Locate every Trypanosoma brucei.
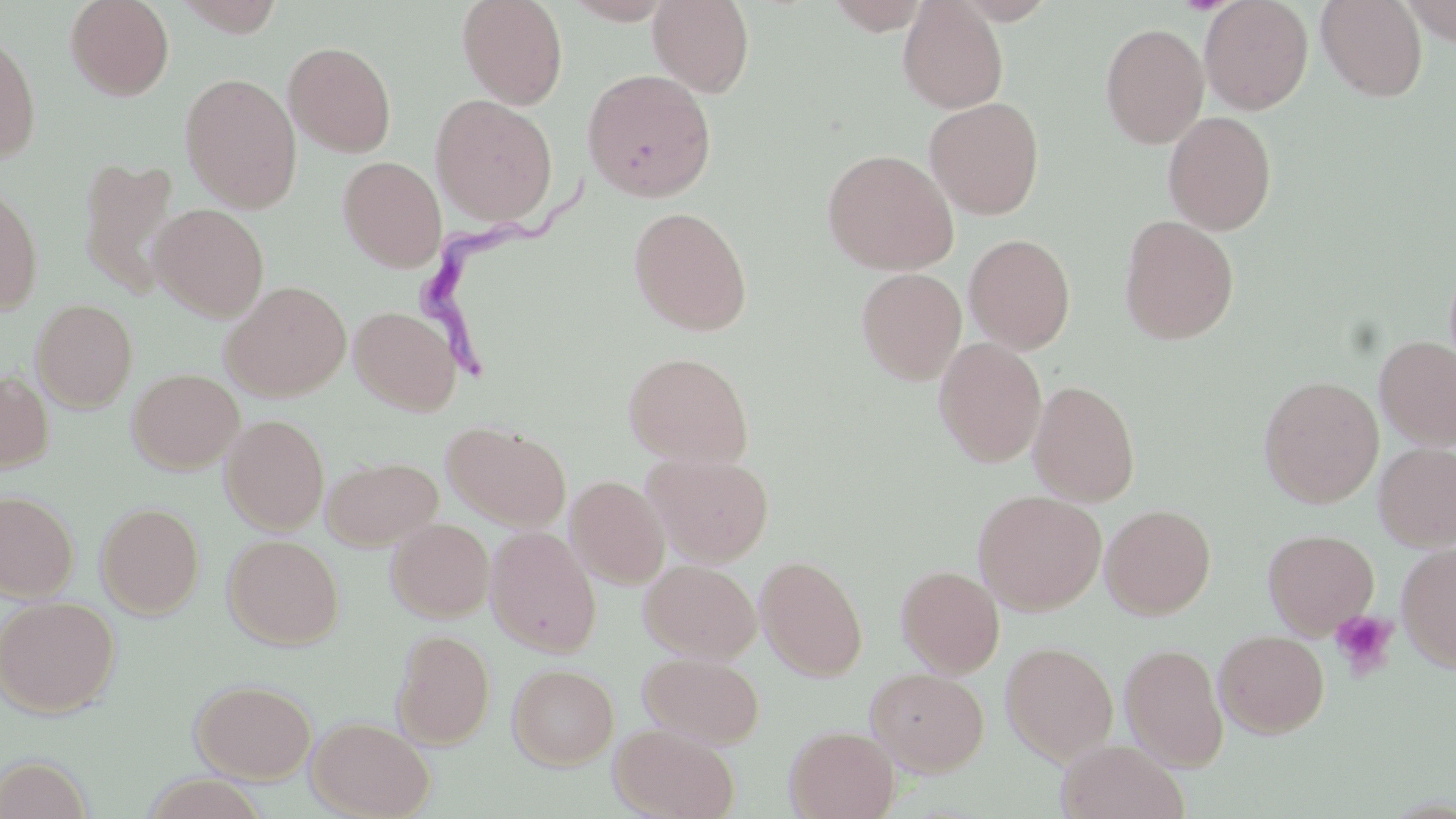
Approximate bounding boxes as (x1,y1)-(x2,y2) corner pairs in pixels.
Trypanosoma brucei: (412,172)-(598,380).

slide_level_diagnosis: Trypanosoma brucei
uninfected_red_blood_cell_locations: 'approximate bounding boxes as (x1,y1)-(x2,y2) corner pairs in pixels: (65,0)-(175,101), (174,0)-(287,38), (457,0)-(569,109), (564,0)-(677,24), (648,0)-(754,97), (826,0)-(932,33), (898,0)-(1009,114), (1199,0)-(1313,114), (1315,0)-(1428,102), (1401,1)-(1454,45), (1100,22)-(1209,148), (0,29)-(41,163), (283,41)-(397,158), (582,69)-(717,203), (180,72)-(302,212), (430,94)-(558,226), (924,97)-(1045,220), (1163,111)-(1277,235), (821,148)-(959,275), (337,156)-(447,271), (78,157)-(181,297), (0,181)-(43,315), (151,203)-(269,321), (628,206)-(752,336), (1118,215)-(1238,345), (964,234)-(1075,354), (856,267)-(967,385), (221,280)-(352,401), (30,299)-(138,413), (349,306)-(462,416), (1374,336)-(1456,450), (933,338)-(1047,468), (622,351)-(754,467), (127,368)-(244,473), (0,370)-(54,472), (1259,375)-(1384,508), (1027,380)-(1140,506), (220,414)-(329,534), (442,420)-(572,531), (1373,443)-(1456,550), (644,451)-(774,566), (322,456)-(442,550), (566,475)-(670,588), (972,489)-(1107,615), (0,490)-(79,601), (96,502)-(205,618), (1100,504)-(1216,618), (386,518)-(494,621), (484,526)-(601,657), (1262,528)-(1379,638), (224,534)-(343,649), (1396,542)-(1456,673), (755,556)-(868,681), (639,559)-(761,662), (896,564)-(1005,678), (0,595)-(120,718), (392,629)-(495,748), (1214,630)-(1329,738), (1001,641)-(1118,764), (1119,642)-(1228,771), (638,651)-(765,748), (507,663)-(619,769), (866,667)-(989,776), (191,678)-(316,783), (307,716)-(435,818), (609,723)-(740,819), (785,726)-(900,819), (1056,738)-(1189,819), (0,754)-(93,819)'
platelet_locations: 'approximate bounding boxes as (x1,y1)-(x2,y2) corner pairs in pixels: (1329,609)-(1400,680)'
field_of_view: single
stain: May-Grünwald-Giemsa
modality: optical microscopy
preparation: thin blood film
magnification: 1000x
image_size: 1456×819 pixels